State the blood parasite species.
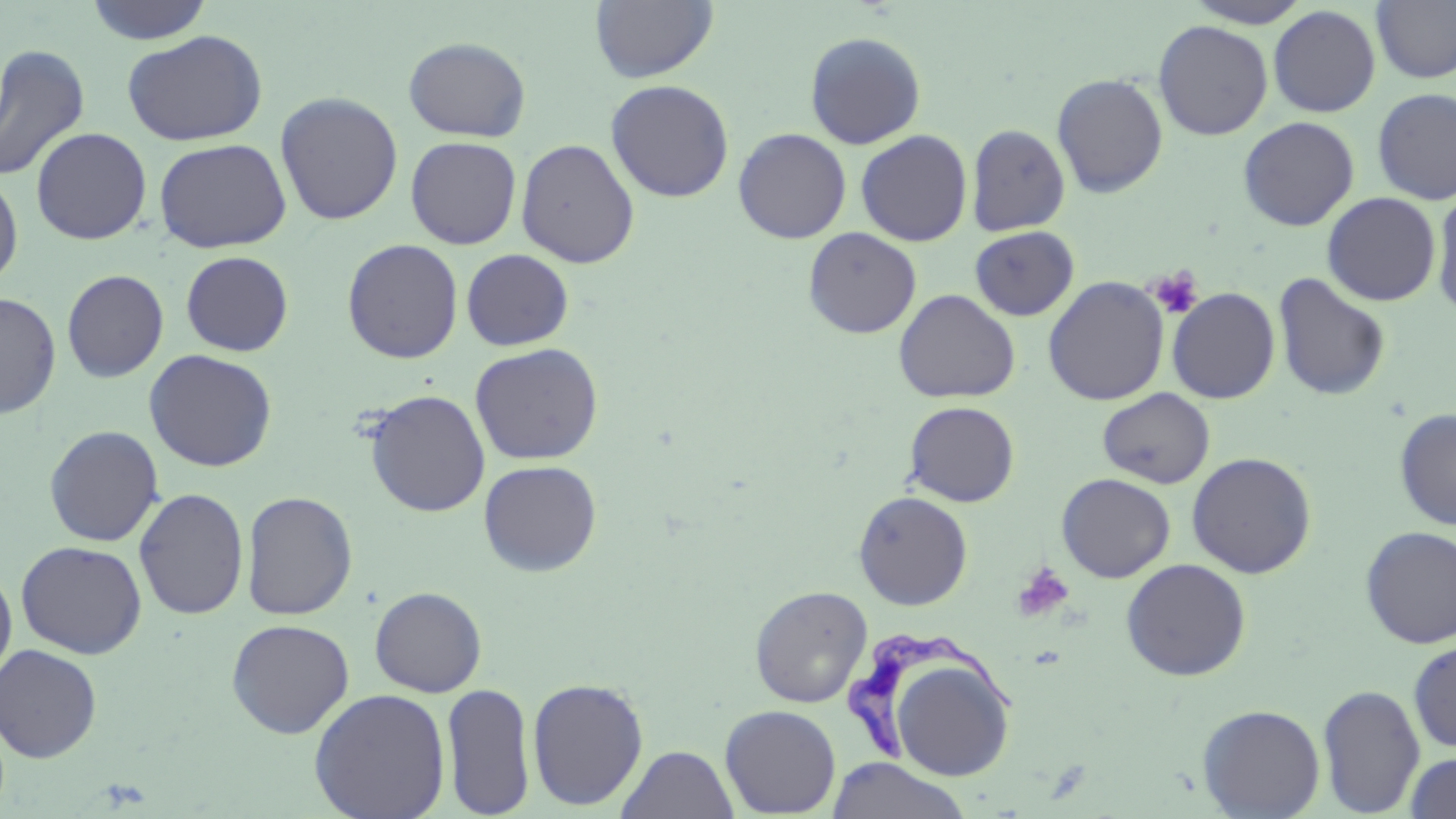
Trypanosoma brucei.

platelet locations = approximate bounding boxes as [x1, y1, x2, y2] in pixels: [1149, 269, 1202, 318], [1011, 562, 1075, 623]
Trypanosoma brucei locations = approximate bounding boxes as [x1, y1, x2, y2] in pixels: [845, 628, 1021, 762]
stain = May-Grünwald-Giemsa
preparation = thin blood smear
magnification = 1000x
uninfected red blood cell locations = approximate bounding boxes as [x1, y1, x2, y2] in pixels: [83, 0, 215, 44], [591, 0, 718, 83], [1372, 0, 1456, 83], [1183, 1, 1312, 28], [1268, 5, 1381, 117], [1153, 20, 1273, 140], [122, 30, 268, 146], [804, 31, 926, 149], [403, 37, 532, 142], [0, 44, 90, 183], [1051, 73, 1168, 198], [605, 79, 735, 203], [1373, 87, 1456, 205], [275, 92, 404, 225], [1238, 116, 1360, 231], [966, 124, 1071, 236], [30, 126, 152, 245], [733, 128, 851, 244], [855, 130, 973, 246], [405, 136, 522, 249], [154, 138, 291, 253], [516, 138, 640, 269], [0, 170, 23, 289], [1432, 185, 1456, 321], [1322, 192, 1440, 306], [969, 225, 1079, 321], [803, 227, 921, 339], [342, 238, 463, 364], [462, 249, 574, 350], [180, 251, 293, 356], [61, 269, 168, 382], [1273, 272, 1391, 401], [1043, 276, 1169, 406], [1166, 287, 1280, 403], [894, 289, 1020, 403], [0, 293, 61, 419], [470, 342, 604, 465], [143, 349, 278, 472], [1097, 387, 1215, 489], [364, 389, 490, 517], [903, 400, 1019, 507], [1393, 408, 1456, 530], [44, 425, 164, 547], [1186, 452, 1317, 578], [478, 459, 603, 577], [1056, 473, 1175, 583], [133, 487, 249, 620], [241, 490, 358, 620], [853, 491, 973, 610], [1359, 525, 1456, 648], [16, 541, 147, 659], [1120, 558, 1252, 681], [0, 564, 17, 685], [369, 586, 487, 697], [749, 586, 872, 708], [226, 618, 355, 739], [1408, 639, 1456, 752], [0, 643, 103, 762], [883, 650, 1017, 782], [527, 677, 649, 810], [441, 682, 535, 817], [1317, 684, 1425, 816], [308, 688, 451, 819], [1197, 704, 1326, 818], [720, 705, 841, 817], [617, 744, 739, 819], [1403, 751, 1456, 819], [826, 757, 972, 819]
modality = optical microscopy
field of view = single
image size = 1456×819 pixels